Identify the parasite.
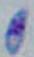
Toxoplasma gondii.

Micrograph. Captured at 1000x magnification.